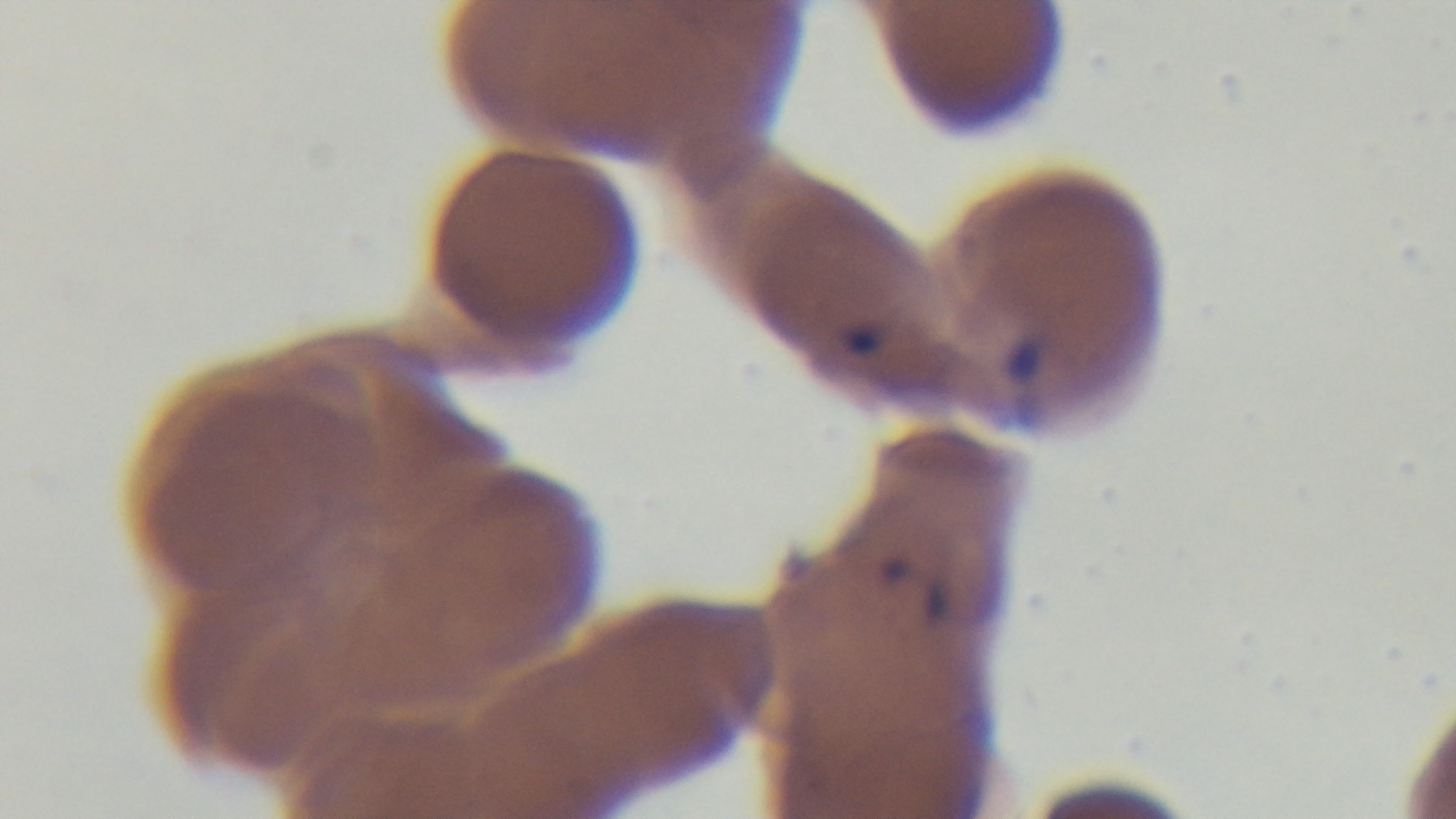 Captured with a mounted 4K digital camera. Giemsa stain. Malaria status: positive. One field from the slide. Preparation: thin smear. Oil-immersion objective, 100x. Photomicrograph.